State the preparation type.
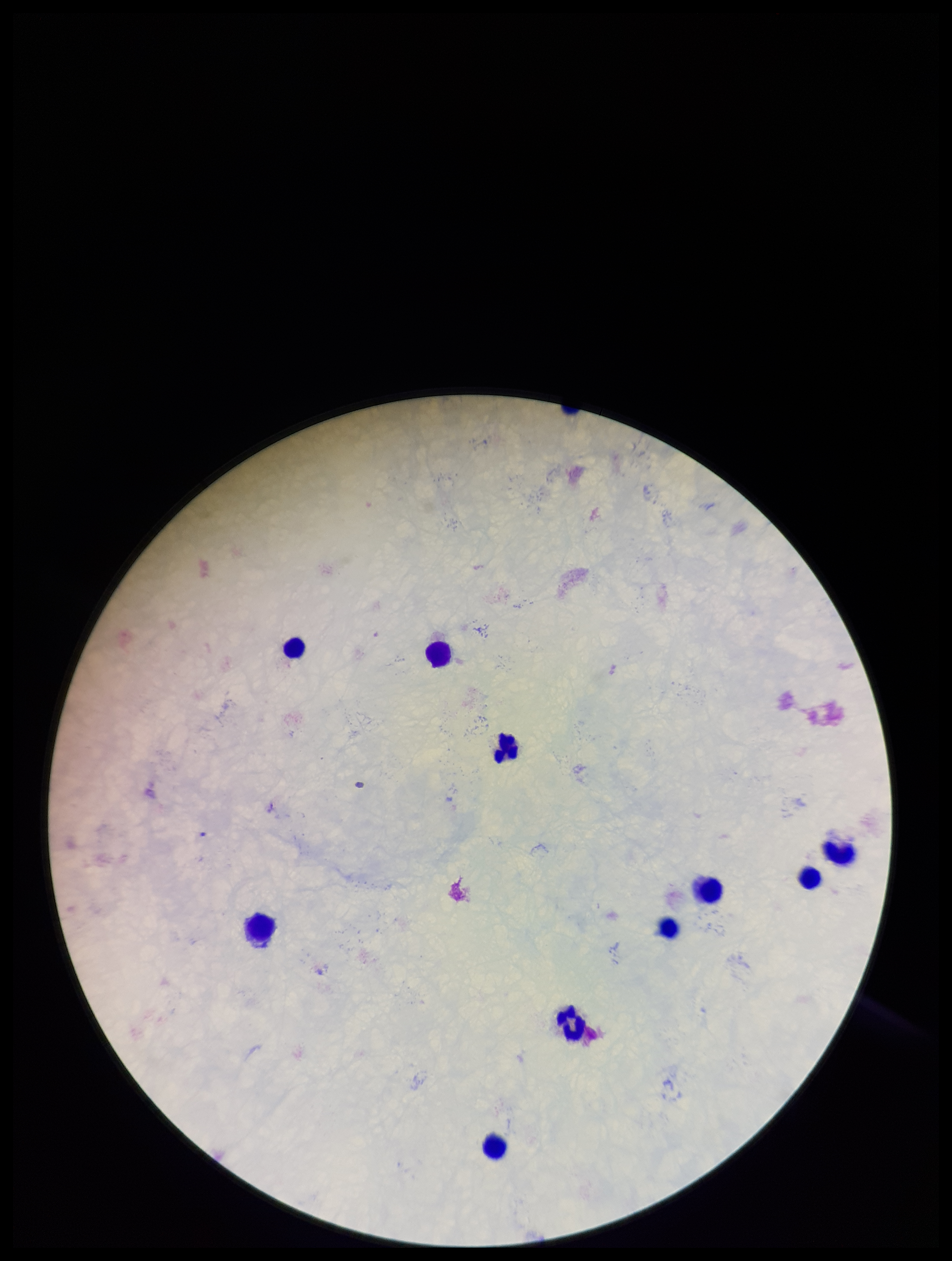
Thick.

Photographed through the microscope eyepiece with a smartphone camera. Leukocyte count: 10. Plasmodium parasites: none seen. Parasite count: 0. One field from this slide. Patient malaria status: negative. Stained with Giemsa. Image is 952×1261 pixels.